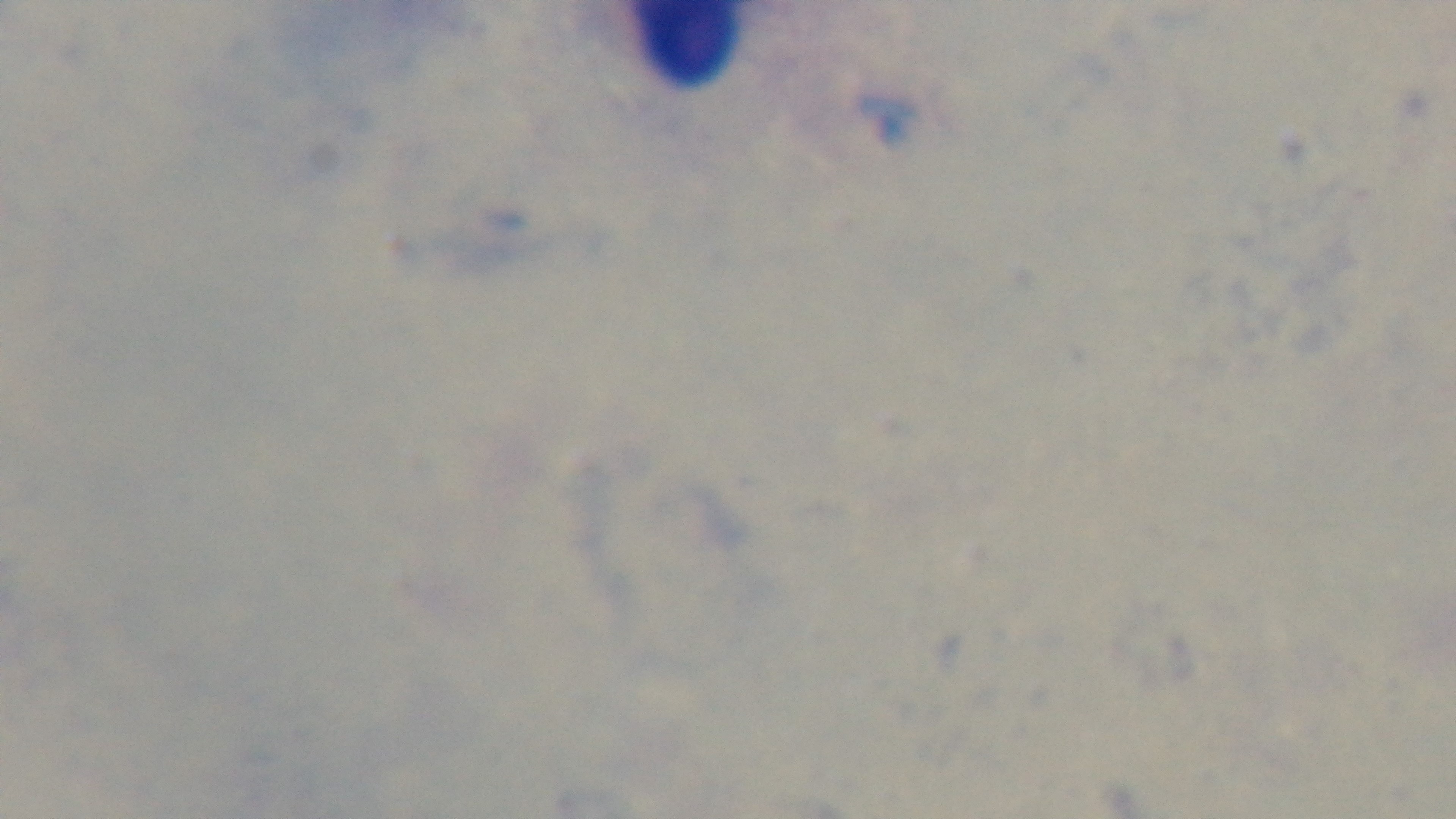
Summary:
  - Objective: 100x oil immersion
  - Stain: Giemsa
  - Field of view: one from the slide
  - Capture: mounted 4K digital camera
  - Preparation: thick blood film
  - Modality: light microscopy
  - Malaria status: uninfected